Describe the morphology of the red blood cells.
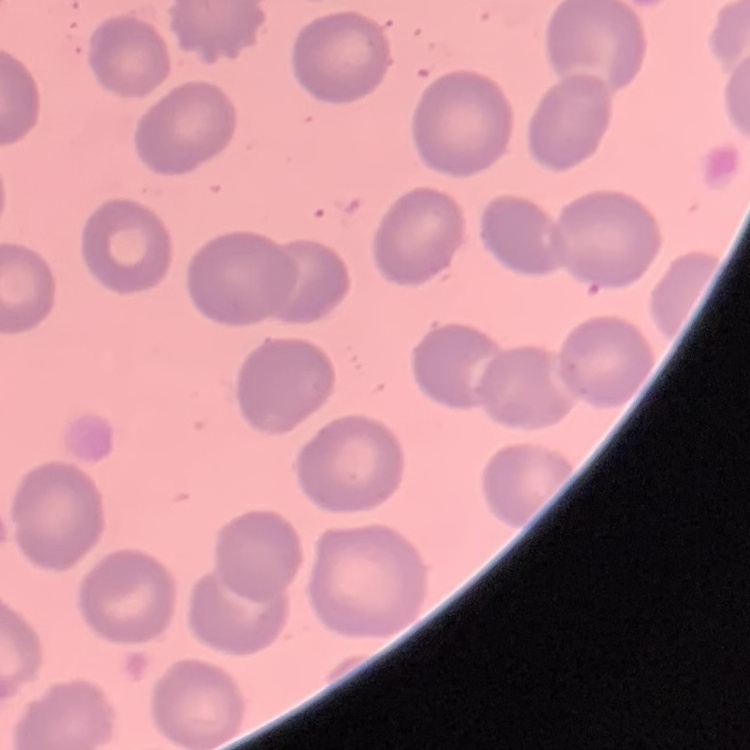
No rouleaux formation.

Thin blood smear. Stained with either Field's or Giemsa. One tile cut from a larger photomicrograph.